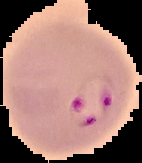
Summary:
  - Image type: segmented cell region on a black background
  - Malaria status: parasitized
  - Image size: 142×163 pixels
  - Preparation: thin blood smear